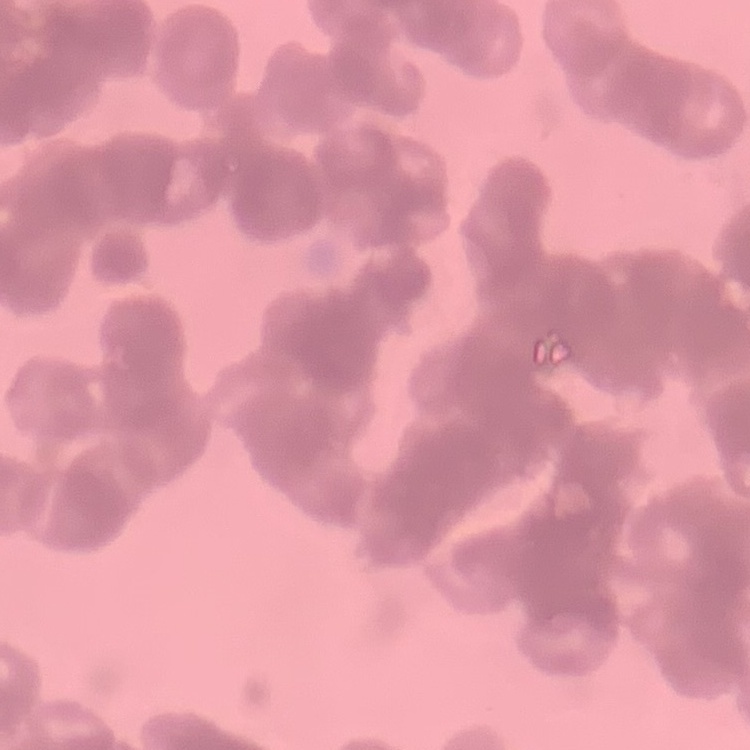
Summary:
  - Erythrocyte morphology: rouleaux formation
  - Stain: Field's or Giemsa
  - Preparation: thin peripheral smear
  - Image type: one tile cut from a larger photomicrograph